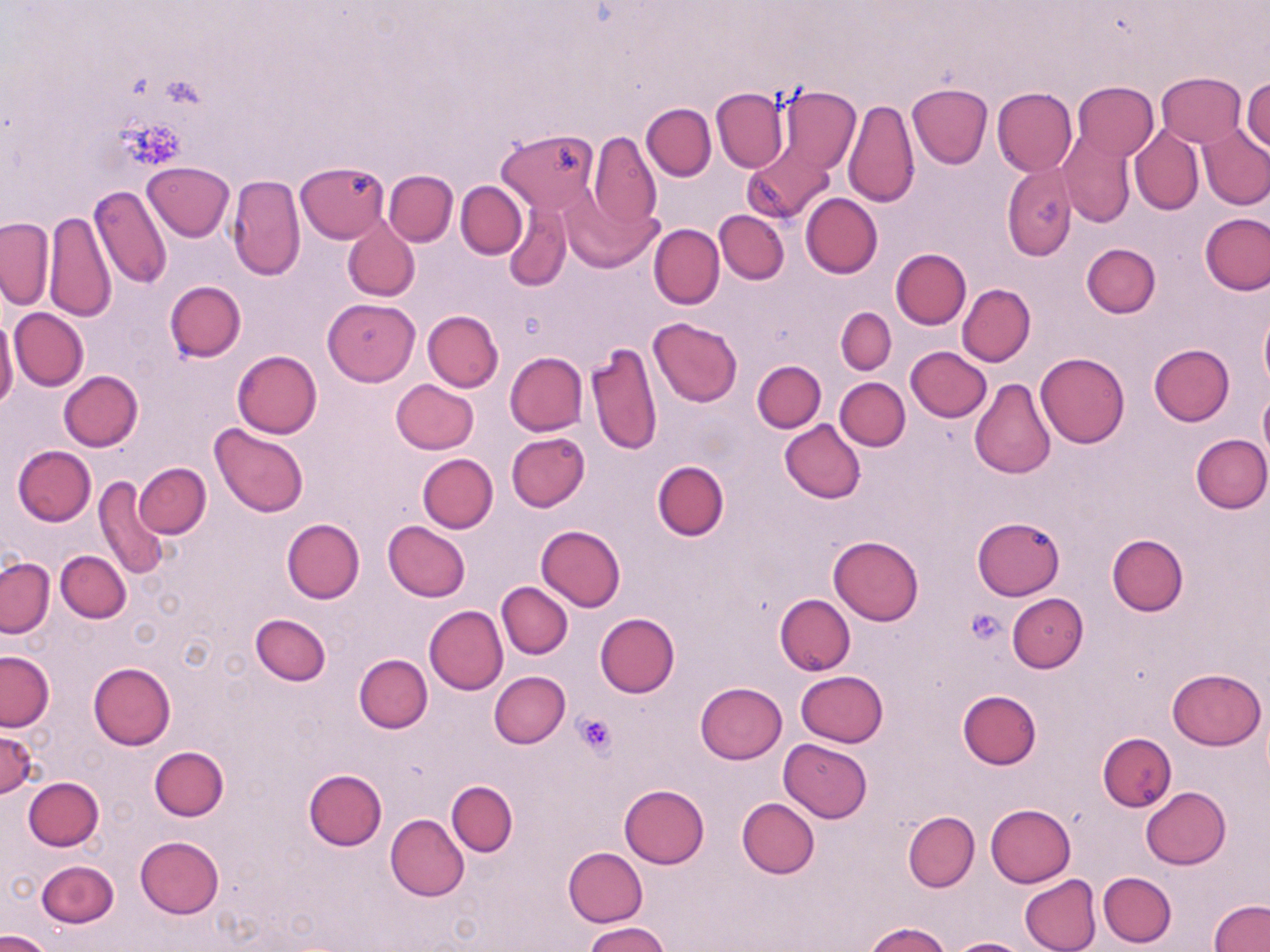
slide-level diagnosis = no evidence of blood parasites
platelet locations = approximate bounding boxes as named x1/y1/x2/y2 corners in pixels: (x1=966, y1=608, x2=1006, y2=643), (x1=574, y1=712, x2=620, y2=758)
uninfected red blood cell locations = approximate bounding boxes as named x1/y1/x2/y2 corners in pixels: (x1=1157, y1=72, x2=1247, y2=146), (x1=1243, y1=80, x2=1270, y2=151), (x1=1072, y1=81, x2=1159, y2=160), (x1=907, y1=83, x2=992, y2=168), (x1=711, y1=86, x2=789, y2=173), (x1=772, y1=86, x2=857, y2=175), (x1=992, y1=87, x2=1078, y2=176), (x1=844, y1=99, x2=919, y2=207), (x1=641, y1=102, x2=716, y2=180), (x1=1199, y1=126, x2=1270, y2=208), (x1=1129, y1=127, x2=1204, y2=215), (x1=497, y1=130, x2=598, y2=213), (x1=1058, y1=131, x2=1135, y2=226), (x1=589, y1=132, x2=662, y2=231), (x1=745, y1=142, x2=834, y2=223), (x1=298, y1=161, x2=389, y2=242), (x1=141, y1=162, x2=233, y2=242), (x1=1004, y1=165, x2=1076, y2=258), (x1=384, y1=170, x2=458, y2=246), (x1=227, y1=175, x2=306, y2=280), (x1=457, y1=181, x2=526, y2=259), (x1=562, y1=185, x2=659, y2=272), (x1=89, y1=186, x2=172, y2=290), (x1=801, y1=193, x2=883, y2=278), (x1=504, y1=199, x2=573, y2=292), (x1=715, y1=210, x2=789, y2=284), (x1=44, y1=211, x2=115, y2=323), (x1=1201, y1=213, x2=1270, y2=295), (x1=342, y1=216, x2=420, y2=301), (x1=1, y1=217, x2=55, y2=309), (x1=649, y1=224, x2=725, y2=309), (x1=1081, y1=243, x2=1160, y2=318), (x1=891, y1=248, x2=971, y2=329), (x1=164, y1=281, x2=245, y2=363), (x1=957, y1=283, x2=1035, y2=366), (x1=322, y1=298, x2=420, y2=386), (x1=836, y1=307, x2=896, y2=375), (x1=9, y1=308, x2=89, y2=390), (x1=423, y1=310, x2=503, y2=392), (x1=1259, y1=311, x2=1270, y2=389), (x1=4, y1=313, x2=35, y2=405), (x1=0, y1=315, x2=18, y2=414), (x1=648, y1=317, x2=742, y2=406), (x1=585, y1=340, x2=663, y2=457), (x1=1149, y1=343, x2=1235, y2=425), (x1=906, y1=347, x2=991, y2=422), (x1=231, y1=350, x2=322, y2=438), (x1=504, y1=351, x2=587, y2=435), (x1=1036, y1=352, x2=1129, y2=448), (x1=752, y1=360, x2=826, y2=432), (x1=59, y1=371, x2=143, y2=450), (x1=836, y1=377, x2=910, y2=449), (x1=969, y1=378, x2=1055, y2=479), (x1=390, y1=379, x2=478, y2=454), (x1=1259, y1=388, x2=1270, y2=465), (x1=779, y1=419, x2=866, y2=504), (x1=211, y1=424, x2=309, y2=518), (x1=506, y1=432, x2=589, y2=512), (x1=1191, y1=434, x2=1270, y2=513), (x1=12, y1=445, x2=96, y2=526), (x1=417, y1=454, x2=497, y2=533), (x1=652, y1=461, x2=730, y2=541), (x1=134, y1=463, x2=211, y2=538), (x1=93, y1=477, x2=170, y2=580), (x1=972, y1=516, x2=1065, y2=600), (x1=281, y1=519, x2=364, y2=603), (x1=382, y1=521, x2=470, y2=602), (x1=536, y1=525, x2=626, y2=611), (x1=1107, y1=533, x2=1189, y2=616), (x1=828, y1=536, x2=924, y2=625), (x1=56, y1=550, x2=129, y2=622), (x1=1, y1=558, x2=54, y2=637), (x1=497, y1=583, x2=573, y2=659), (x1=774, y1=593, x2=855, y2=674), (x1=1007, y1=593, x2=1088, y2=672), (x1=424, y1=605, x2=507, y2=695), (x1=251, y1=613, x2=330, y2=686), (x1=595, y1=613, x2=680, y2=697), (x1=0, y1=651, x2=54, y2=731), (x1=353, y1=654, x2=432, y2=733), (x1=88, y1=662, x2=176, y2=749), (x1=1168, y1=667, x2=1265, y2=750), (x1=488, y1=671, x2=570, y2=748), (x1=796, y1=671, x2=888, y2=747), (x1=694, y1=682, x2=787, y2=764), (x1=958, y1=690, x2=1042, y2=769), (x1=0, y1=729, x2=39, y2=798), (x1=1098, y1=733, x2=1177, y2=812), (x1=779, y1=739, x2=872, y2=822), (x1=149, y1=747, x2=228, y2=821), (x1=304, y1=768, x2=387, y2=850), (x1=24, y1=778, x2=103, y2=851), (x1=446, y1=780, x2=518, y2=856), (x1=619, y1=785, x2=709, y2=867), (x1=1142, y1=788, x2=1230, y2=869), (x1=737, y1=798, x2=819, y2=878), (x1=985, y1=804, x2=1076, y2=887), (x1=903, y1=811, x2=980, y2=891), (x1=386, y1=814, x2=470, y2=900), (x1=135, y1=836, x2=224, y2=918), (x1=564, y1=847, x2=648, y2=926), (x1=36, y1=860, x2=118, y2=928), (x1=1098, y1=872, x2=1177, y2=947), (x1=1018, y1=874, x2=1100, y2=952), (x1=1209, y1=900, x2=1270, y2=952), (x1=585, y1=922, x2=671, y2=952), (x1=864, y1=922, x2=953, y2=952), (x1=1, y1=931, x2=53, y2=952), (x1=945, y1=938, x2=1032, y2=952)
magnification = 1000x
image size = 1270×952 pixels
preparation = thin blood smear
stain = May-Grünwald-Giemsa
modality = optical microscopy
field of view = one of a larger specimen